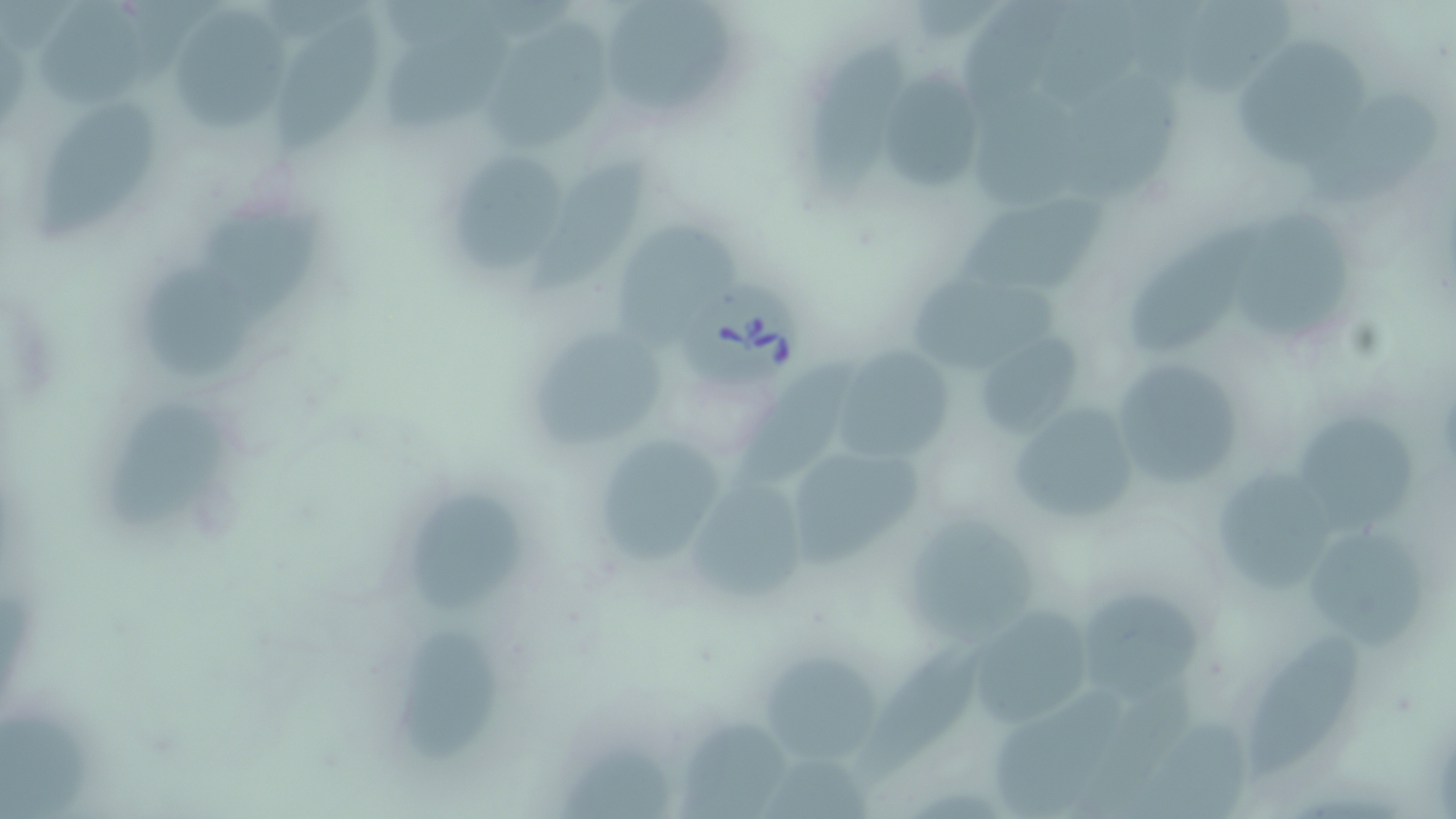

{
  "slide_level_diagnosis": "Babesia divergens",
  "field_of_view": "one of a larger specimen",
  "preparation": "thin blood smear",
  "magnification": "1000x",
  "uninfected_red_blood_cell_locations": "approximate bounding boxes as [x1, y1, x2, y2] in pixels: [31, 0, 144, 113], [602, 0, 727, 111], [175, 5, 287, 127], [272, 9, 383, 151], [381, 18, 514, 132], [487, 22, 605, 153], [1233, 34, 1372, 174], [814, 41, 905, 193], [883, 65, 988, 193], [1071, 68, 1191, 200], [955, 77, 1094, 208], [1311, 89, 1445, 205], [35, 106, 157, 238], [459, 152, 567, 273], [531, 156, 652, 295], [956, 193, 1108, 294], [209, 198, 328, 322], [1234, 211, 1355, 339], [617, 224, 738, 335], [1133, 227, 1263, 354], [143, 261, 255, 379], [912, 268, 1061, 373], [970, 324, 1092, 448], [534, 325, 669, 450], [836, 349, 954, 457], [1097, 352, 1253, 492], [738, 358, 851, 483], [1006, 398, 1148, 531], [110, 401, 214, 533], [1295, 407, 1418, 537], [597, 441, 725, 566], [777, 443, 927, 568], [1215, 466, 1341, 591], [690, 475, 803, 603], [402, 490, 531, 611], [907, 514, 1043, 646], [1310, 525, 1429, 654], [1080, 582, 1205, 705], [967, 603, 1094, 731], [400, 621, 498, 765], [1251, 632, 1363, 772], [864, 643, 976, 780], [759, 650, 885, 761], [996, 683, 1131, 819], [0, 705, 86, 819], [1139, 715, 1247, 819], [681, 719, 792, 819], [551, 738, 677, 819]",
  "modality": "light microscopy",
  "image_size": "1456×819 pixels",
  "babesia_divergens_infected_red_blood_cell_locations": "approximate bounding boxes as [x1, y1, x2, y2] in pixels: [682, 278, 810, 390]",
  "stain": "May-Grünwald-Giemsa"
}